Assess for malaria.
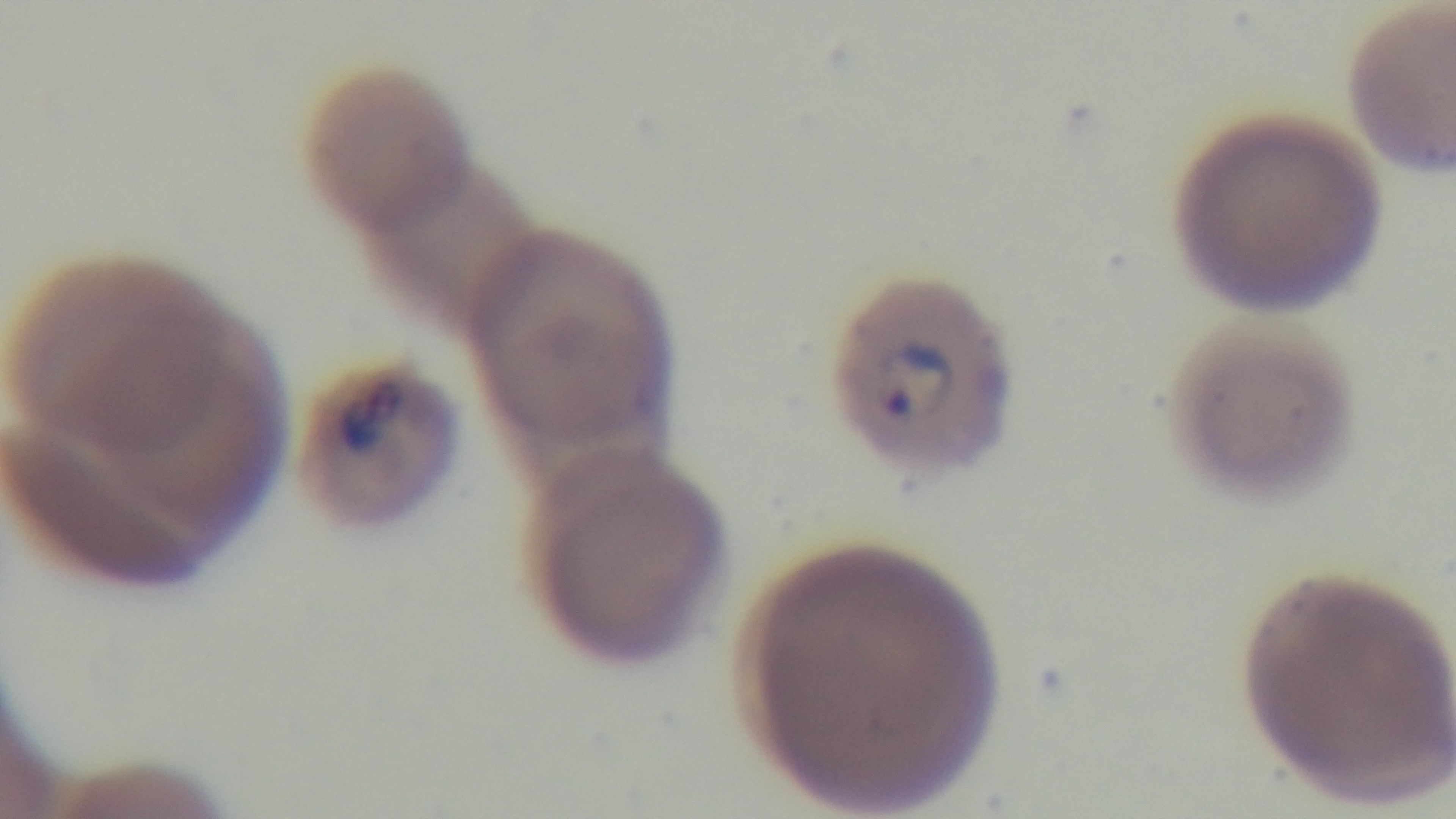
Positive.

Summary:
  - Modality: light microscopy
  - Capture: mounted 4K digital camera
  - Stain: Giemsa
  - Preparation: thin
  - Objective: 100x oil immersion
  - Field of view: single